Assess this cell for malaria.
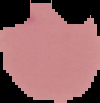

Parasitized.

preparation = thin blood film
image type = segmented cell region with the area outside set to black
image size = 100×103 pixels